Assess this cell for malaria.
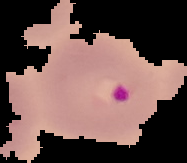

It is parasitized.

Summary:
  - Image type: segmented cell region on a black background
  - Image size: 187×163 pixels
  - Preparation: thin blood smear